Report the malaria status of this cell.
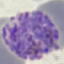

Parasitized.

Giemsa-stained preparation. Acquired by smartphone through the microscope eyepiece. Cell patch, automatically extracted from a larger field of view and resized to 64 × 64 pixels. Thin smear of blood.